Assess the morphology of the erythrocytes.
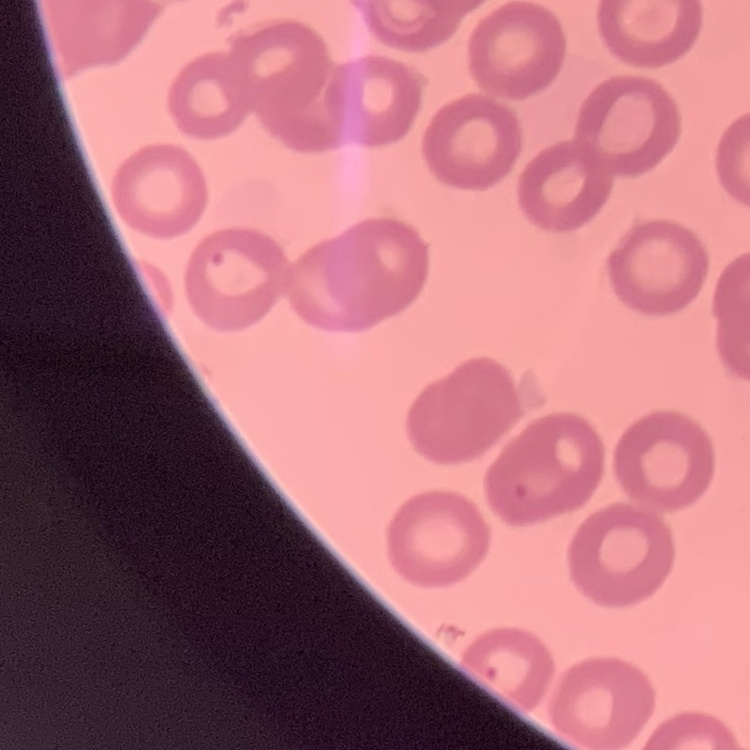
They show no rouleaux formation.

One tile cut from a larger photomicrograph. Stained with either Field's or Giemsa. Thin blood film.